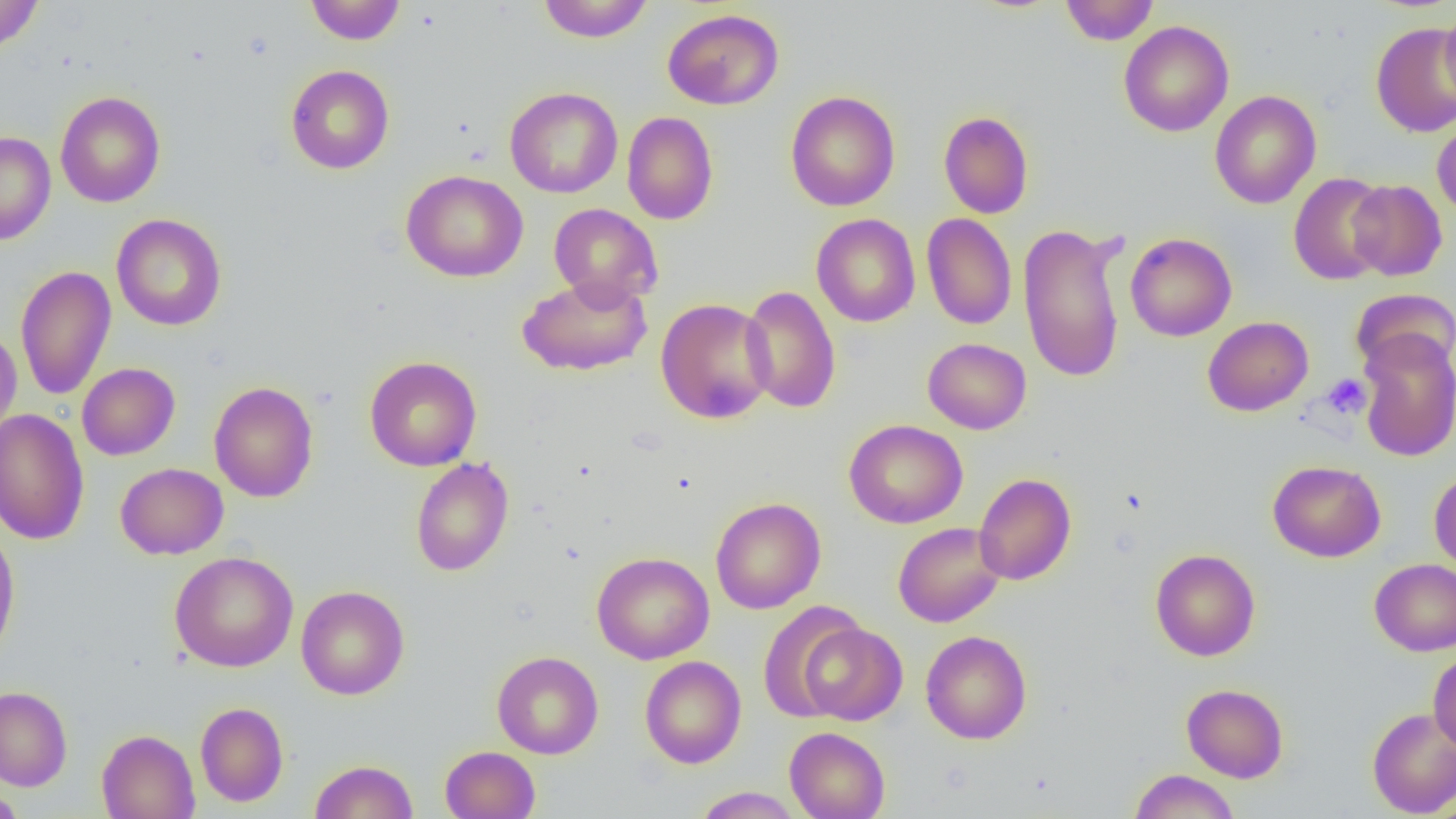
Summary:
  - Coordinate format: approximate bounding boxes as (x1,y1)-(x2,y2) corner pairs in pixels
  - Platelet locations: (1322,373)-(1371,419)
  - Uninfected red blood cell locations: (0,0)-(44,55), (304,0)-(405,44), (537,0)-(655,43), (1059,0)-(1159,45), (1439,5)-(1456,104), (662,8)-(784,110), (1119,20)-(1234,137), (1370,22)-(1456,137), (286,64)-(394,174), (504,86)-(623,198), (785,90)-(900,212), (1209,90)-(1322,209), (55,91)-(165,207), (622,111)-(719,225), (938,111)-(1034,218), (1432,117)-(1456,222), (0,131)-(56,245), (401,170)-(528,282), (1289,172)-(1391,285), (1347,179)-(1448,281), (549,203)-(663,307), (111,213)-(227,331), (811,213)-(921,327), (921,213)-(1016,330), (1018,222)-(1128,384), (1125,233)-(1237,341), (15,265)-(116,400), (516,273)-(653,377), (740,285)-(841,413), (1350,288)-(1456,378), (656,298)-(776,424), (1202,316)-(1314,416), (0,327)-(22,439), (1357,328)-(1456,462), (923,338)-(1031,434), (364,356)-(481,471), (77,363)-(180,460), (209,381)-(319,502), (0,409)-(90,544), (844,419)-(968,528), (410,457)-(514,576), (1268,460)-(1385,562), (115,463)-(228,559), (1429,469)-(1456,574), (973,473)-(1077,585), (710,497)-(826,614), (893,522)-(1005,627), (0,526)-(20,664), (1150,548)-(1260,661), (170,551)-(299,672), (592,551)-(714,664), (1369,558)-(1456,656), (296,585)-(409,700), (758,600)-(866,720), (797,621)-(907,725), (920,630)-(1032,744), (491,651)-(604,759), (1428,651)-(1456,752), (640,655)-(746,769), (1181,683)-(1289,783), (0,686)-(72,790), (195,702)-(289,807), (1366,707)-(1456,818), (784,727)-(890,819), (96,729)-(200,819), (440,745)-(541,818), (309,759)-(418,819), (1129,769)-(1240,819), (692,786)-(803,818), (0,789)-(27,818)
  - Slide-level diagnosis: negative for blood parasites
  - Image size: 1456×819 pixels
  - Preparation: thin blood film
  - Magnification: 1000x
  - Field of view: one of a larger specimen
  - Modality: optical microscopy